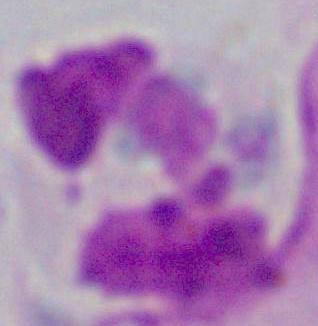

{
  "identification": "white blood cell",
  "modality": "photomicrograph",
  "magnification": "1000x"
}